State which parasite is depicted.
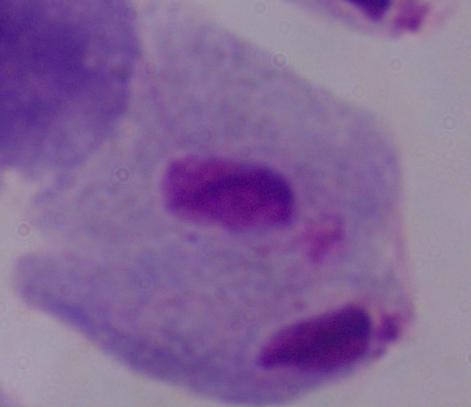

A trichomonad.

Summary:
  - Modality: micrograph
  - Magnification: 1000x